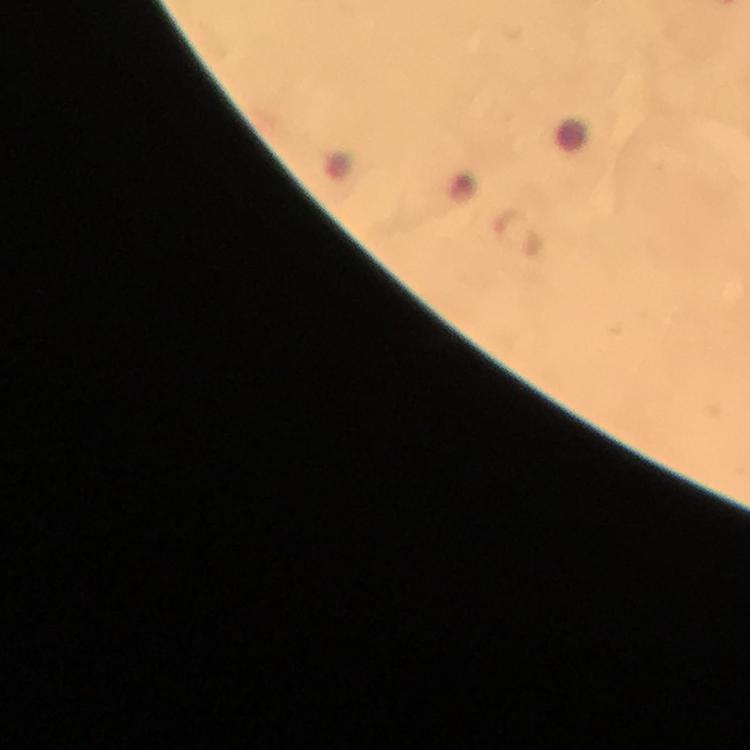

Approximate object centers, in pixels from the top-left corner.
Summary:
  - Malaria parasite locations: (x=519, y=233)
  - Cropped from: one field of view
  - Capture: smartphone mounted on the microscope
  - Magnification: 100x
  - Stain: Giemsa
  - Immersion oil: applied
  - Preparation: thick blood smear
  - Image size: 750×750 pixels
  - Context: from a malaria diagnostic workup